Describe the morphology of the red blood cells.
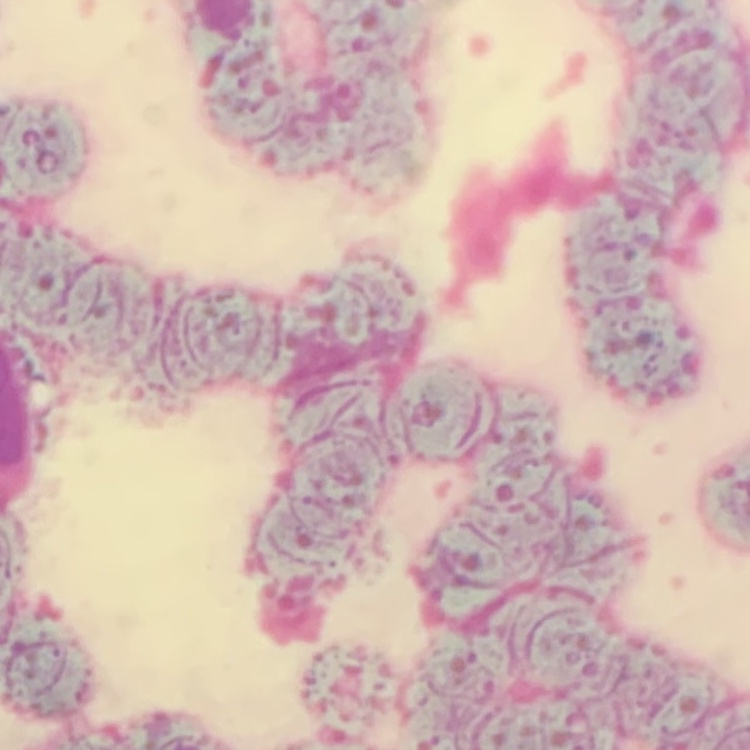

Rouleaux formation.

{
  "stain": "Field's or Giemsa",
  "preparation": "thin blood film",
  "image_type": "square crop of a larger photomicrograph"
}